Outline each Babesia divergens-infected red blood cell.
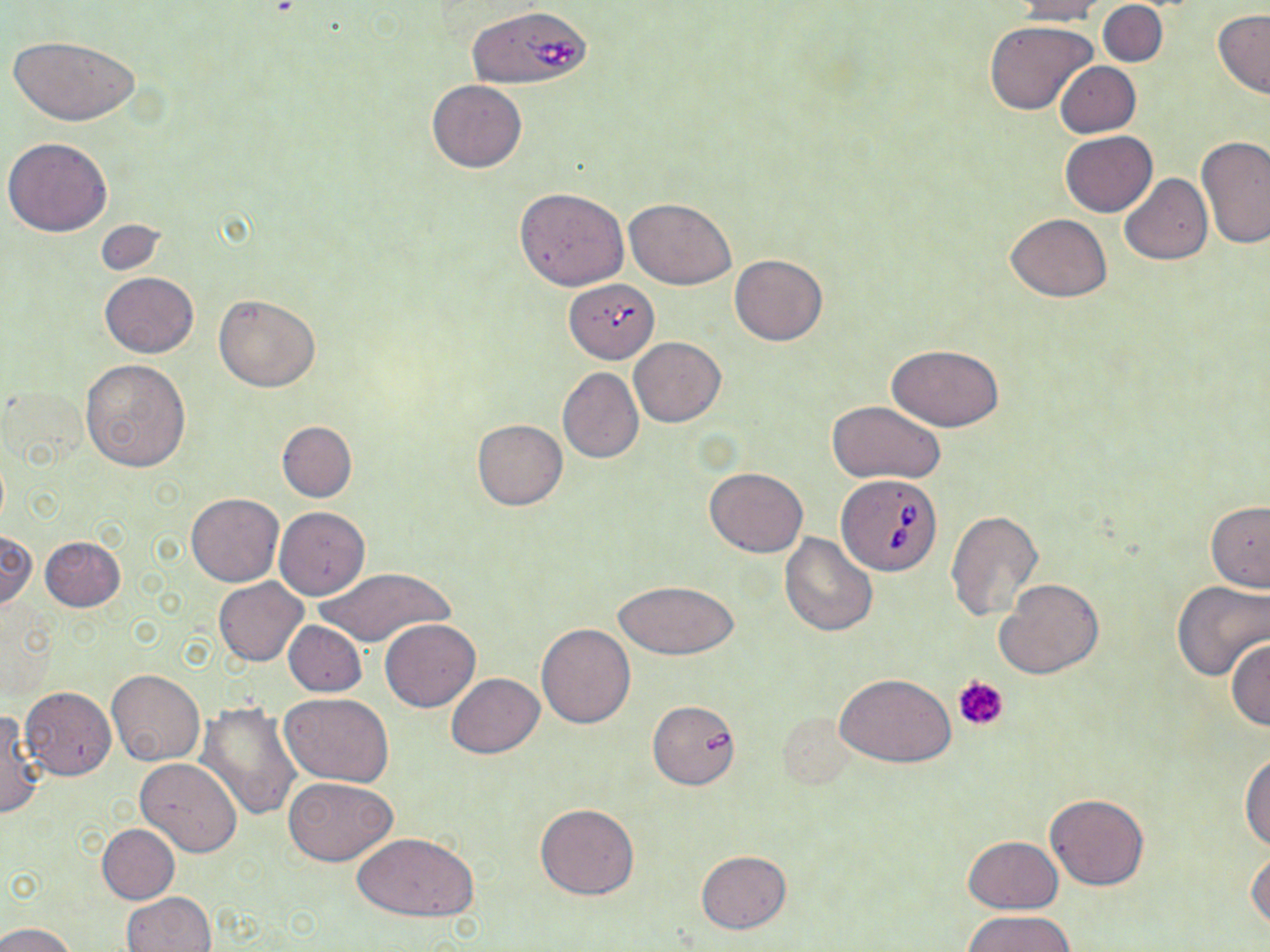
Approximate bounding boxes as [x1, y1, x2, y2] in pixels.
Babesia divergens-infected red blood cells: [467, 5, 593, 90], [566, 280, 658, 363], [837, 474, 943, 576].

Summary:
  - Platelet locations: [953, 675, 1009, 731]
  - Uninfected red blood cell locations: [1010, 0, 1110, 23], [1098, 1, 1167, 67], [1214, 10, 1270, 99], [985, 21, 1097, 116], [9, 35, 139, 126], [1055, 61, 1140, 137], [428, 79, 526, 172], [1060, 131, 1157, 215], [4, 136, 112, 236], [1197, 137, 1270, 251], [1120, 174, 1213, 264], [515, 188, 628, 290], [626, 197, 735, 290], [1005, 213, 1112, 302], [92, 219, 168, 275], [730, 254, 827, 346], [99, 272, 197, 357], [213, 295, 320, 392], [629, 337, 726, 427], [886, 343, 1003, 431], [80, 359, 192, 473], [558, 368, 644, 464], [3, 383, 91, 471], [827, 400, 944, 484], [472, 419, 567, 511], [277, 420, 356, 502], [705, 468, 808, 557], [186, 493, 282, 586], [1206, 500, 1270, 591], [275, 506, 369, 599], [946, 511, 1042, 622], [1, 530, 38, 610], [780, 533, 877, 635], [40, 535, 125, 611], [314, 565, 454, 648], [214, 578, 308, 666], [996, 578, 1104, 680], [613, 580, 739, 660], [1172, 580, 1270, 681], [380, 619, 480, 712], [282, 620, 368, 696], [536, 623, 635, 728], [1226, 638, 1270, 731], [106, 669, 205, 766], [446, 673, 543, 758], [837, 673, 955, 767], [20, 686, 117, 780], [280, 693, 394, 787], [648, 701, 739, 789], [196, 702, 304, 822], [0, 709, 43, 819], [775, 711, 856, 789], [1240, 750, 1270, 851], [136, 757, 242, 857], [283, 776, 397, 865], [1045, 793, 1148, 890], [534, 804, 640, 900], [98, 824, 179, 903], [351, 832, 480, 921], [963, 837, 1063, 912], [1248, 848, 1270, 934], [697, 850, 790, 933], [122, 892, 215, 952], [964, 911, 1074, 951], [0, 922, 76, 952]
  - Slide-level diagnosis: Babesia divergens
  - Image size: 1270×952 pixels
  - Stain: May-Grünwald-Giemsa
  - Modality: optical microscopy
  - Preparation: thin blood film
  - Magnification: 1000x
  - Field of view: single